Classify this cell by malaria status.
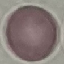
It is uninfected.

Summary:
  - Preparation: thin blood film
  - Stain: Giemsa
  - Image type: cell patch, automatically extracted from a larger field of view and resized to 64 × 64 pixels
  - Capture: smartphone through the microscope eyepiece